Comment on the morphology of the red blood cells.
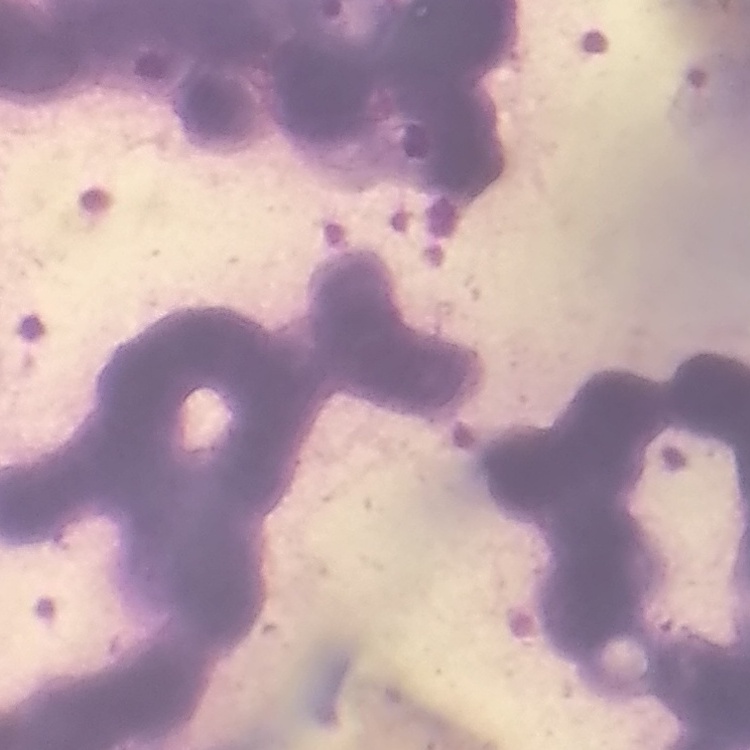

Rouleaux formation.

stain = Field's or Giemsa
preparation = thin blood smear
image type = square crop of a larger photomicrograph